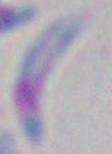
Micrograph. Toxoplasma gondii is seen. Captured at 1000x magnification.